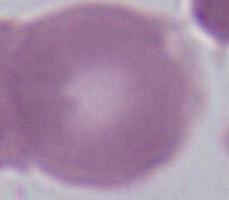
A red blood cell is seen. 1000x magnification. Photomicrograph.